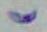
Summary:
  - Magnification: 1000x
  - Modality: micrograph
  - Identification: Toxoplasma gondii